State the preparation type.
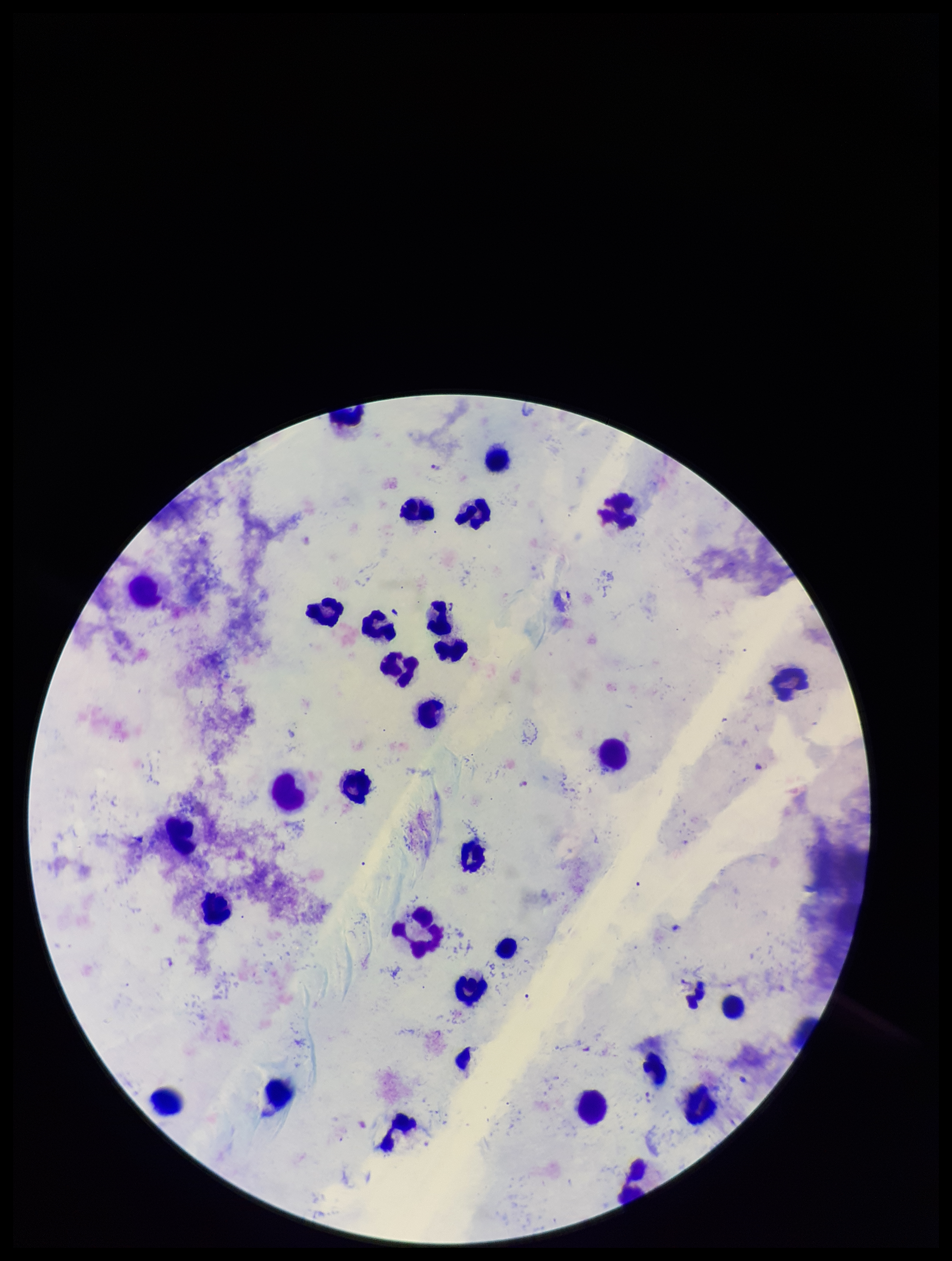

A thick smear.

Photographed through the microscope eyepiece with a smartphone camera. Parasite count: 3. Species reported for this patient: Plasmodium falciparum. Giemsa stain. Image is 952×1261 pixels. Leukocyte count: 30. Patient malaria status: infected. Plasmodium parasites: seen. Single field of view.